Give the location of every parasitized red blood cell.
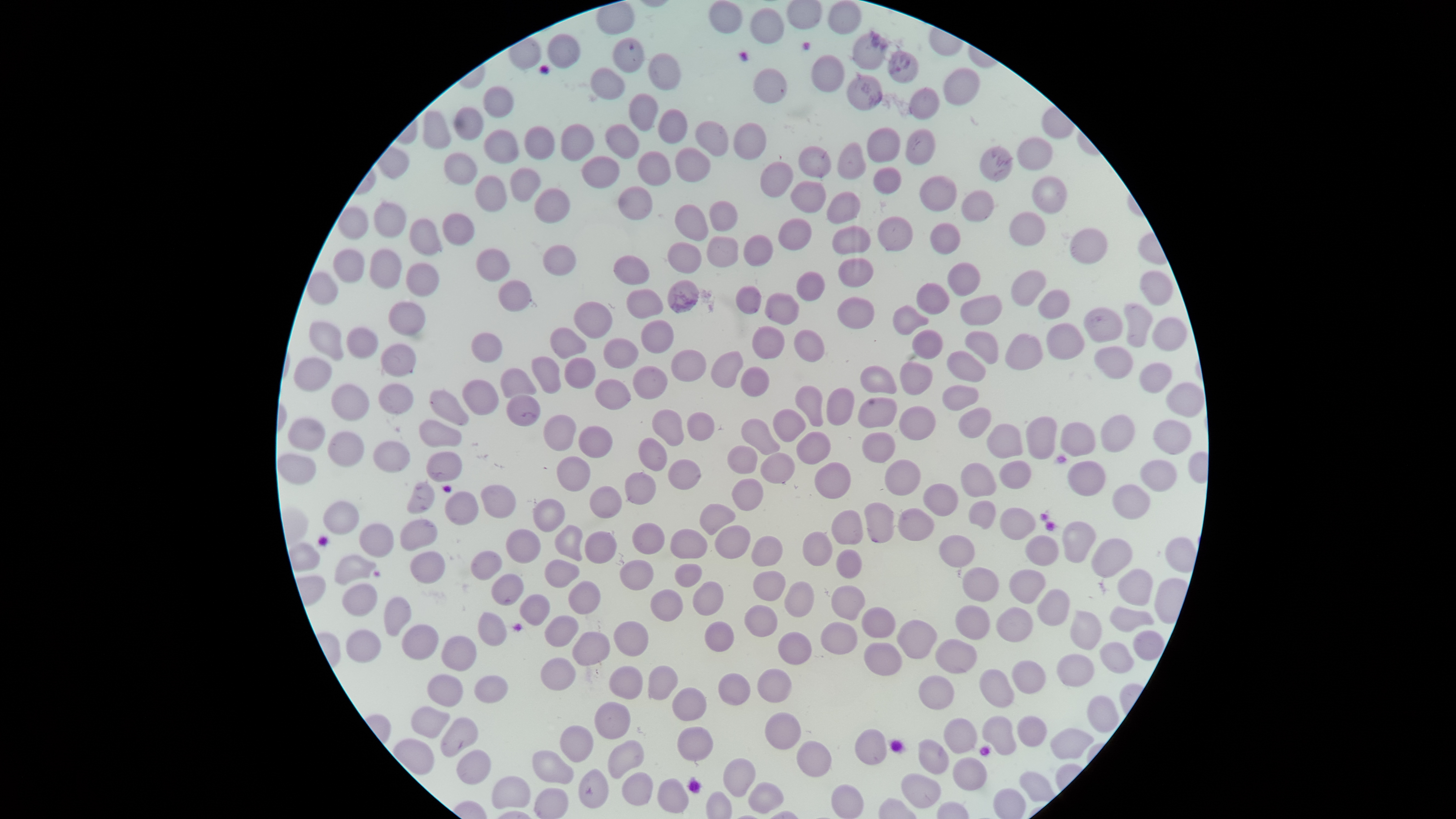
No parasitized red blood cells identified.

Approximate bounding boxes as {left, top, right, bottom} in pixels. Uninfected red blood cells: {828, 0, 863, 35}, {709, 1, 743, 34}, {750, 8, 785, 45}, {852, 32, 888, 71}, {547, 33, 580, 69}, {887, 51, 918, 84}, {648, 53, 681, 90}, {811, 55, 845, 92}, {589, 68, 625, 100}, {753, 68, 787, 104}, {943, 68, 981, 106}, {846, 75, 883, 111}, {482, 87, 515, 118}, {908, 88, 940, 121}, {628, 94, 658, 132}, {454, 107, 484, 142}, {657, 108, 687, 145}, {422, 111, 451, 150}, {694, 120, 729, 157}, {732, 122, 767, 160}, {561, 124, 594, 162}, {604, 124, 640, 158}, {523, 126, 554, 161}, {866, 128, 900, 163}, {905, 128, 935, 166}, {484, 129, 518, 165}, {1016, 137, 1053, 170}, {836, 141, 866, 180}, {798, 145, 831, 178}, {978, 146, 1013, 181}, {674, 147, 710, 182}, {637, 151, 671, 186}, {443, 152, 476, 186}, {580, 156, 620, 189}, {760, 160, 793, 198}, {509, 167, 540, 203}, {872, 167, 901, 195}, {475, 175, 506, 212}, {919, 175, 956, 212}, {1031, 175, 1067, 214}, {790, 180, 826, 213}, {618, 186, 652, 220}, {534, 188, 571, 225}, {961, 190, 994, 223}, {826, 192, 861, 224}, {709, 200, 737, 230}, {373, 201, 405, 239}, {673, 204, 709, 241}, {337, 206, 369, 240}, {1008, 211, 1044, 245}, {442, 213, 475, 246}, {876, 216, 913, 252}, {409, 218, 442, 256}, {778, 218, 811, 251}, {929, 223, 962, 255}, {832, 225, 871, 254}, {1069, 228, 1107, 264}, {742, 234, 773, 267}, {706, 236, 738, 267}, {667, 242, 703, 273}, {543, 244, 576, 276}, {476, 248, 509, 283}, {333, 249, 364, 284}, {369, 250, 401, 290}, {612, 255, 649, 284}, {837, 258, 873, 287}, {406, 262, 439, 298}, {947, 262, 981, 297}, {1140, 269, 1173, 306}, {307, 270, 338, 306}, {1010, 270, 1047, 306}, {796, 271, 825, 302}, {498, 279, 530, 312}, {667, 279, 698, 313}, {917, 283, 949, 315}, {735, 285, 762, 315}, {627, 288, 663, 319}, {1038, 289, 1070, 320}, {764, 293, 800, 326}, {960, 295, 1003, 325}, {837, 296, 874, 330}, {573, 301, 612, 339}, {388, 302, 426, 336}, {1123, 303, 1151, 348}, {893, 304, 929, 335}, {1083, 307, 1122, 343}, {1152, 317, 1187, 352}, {640, 319, 675, 354}, {309, 321, 344, 362}, {1046, 323, 1085, 359}, {751, 325, 785, 359}, {550, 327, 587, 359}, {346, 328, 379, 359}, {793, 329, 826, 362}, {911, 330, 943, 359}, {964, 330, 998, 365}, {470, 332, 502, 363}, {1004, 333, 1043, 371}, {603, 338, 638, 369}, {380, 343, 417, 378}, {1093, 346, 1133, 379}, {670, 348, 706, 382}, {711, 351, 743, 388}, {946, 351, 986, 381}, {531, 356, 561, 393}, {293, 357, 333, 392}, {564, 357, 595, 388}, {899, 361, 932, 395}, {1139, 362, 1172, 394}, {632, 365, 668, 400}, {859, 365, 897, 394}, {739, 366, 769, 397}, {500, 368, 535, 398}, {593, 378, 632, 410}, {463, 379, 498, 415}, {378, 383, 414, 415}, {1165, 383, 1204, 418}, {331, 384, 369, 421}, {794, 385, 823, 427}, {941, 385, 979, 411}, {826, 387, 854, 426}, {429, 389, 469, 427}, {506, 394, 541, 426}, {858, 397, 898, 428}, {899, 406, 936, 442}, {958, 407, 991, 439}, {651, 408, 684, 446}, {773, 408, 805, 442}, {686, 412, 715, 442}, {543, 414, 577, 451}, {1100, 414, 1136, 453}, {1025, 416, 1056, 459}, {287, 417, 325, 451}, {741, 418, 780, 456}, {419, 420, 462, 448}, {1152, 420, 1193, 456}, {1060, 422, 1095, 457}, {987, 423, 1023, 459}, {578, 425, 612, 459}, {796, 431, 831, 464}, {327, 432, 364, 467}, {861, 432, 896, 463}, {637, 437, 668, 471}, {373, 441, 410, 473}, {426, 451, 462, 483}, {277, 453, 317, 485}, {760, 453, 795, 484}, {556, 456, 590, 493}, {668, 459, 701, 490}, {1139, 459, 1177, 493}, {884, 460, 921, 495}, {999, 460, 1032, 490}, {1067, 461, 1105, 496}, {815, 462, 852, 499}, {960, 463, 996, 498}, {624, 472, 656, 505}, {730, 478, 763, 510}, {406, 482, 436, 515}, {480, 484, 516, 519}, {923, 484, 958, 516}, {1113, 484, 1151, 520}, {588, 486, 622, 518}, {445, 491, 479, 526}, {532, 499, 566, 532}, {968, 500, 996, 530}, {322, 501, 359, 535}, {864, 502, 894, 543}, {699, 504, 736, 535}, {999, 507, 1036, 541}, {897, 508, 935, 541}, {831, 509, 863, 545}, {399, 520, 439, 551}, {1063, 521, 1097, 563}, {631, 522, 665, 555}, {358, 524, 395, 558}, {553, 524, 583, 561}, {714, 525, 751, 559}, {505, 529, 540, 564}, {669, 529, 708, 560}, {584, 531, 618, 563}, {802, 531, 833, 566}, {750, 535, 783, 567}, {938, 535, 975, 567}, {1024, 536, 1060, 566}, {1091, 538, 1132, 579}, {835, 549, 862, 578}, {470, 550, 503, 581}, {410, 551, 446, 584}, {334, 554, 376, 585}, {544, 559, 580, 589}, {618, 559, 654, 591}, {674, 563, 703, 588}, {962, 567, 999, 601}, {1117, 569, 1153, 606}, {753, 570, 785, 601}, {1009, 570, 1045, 604}, {491, 573, 524, 606}, {692, 580, 724, 616}, {568, 581, 600, 615}, {783, 581, 815, 618}, {342, 583, 378, 618}, {830, 585, 866, 621}, {650, 588, 683, 622}, {1035, 589, 1070, 627}, {519, 594, 550, 626}, {383, 596, 412, 639}, {744, 604, 778, 637}, {954, 605, 991, 640}, {1109, 606, 1153, 633}, {860, 607, 895, 639}, {995, 607, 1033, 642}, {1070, 611, 1102, 650}, {477, 612, 507, 647}, {544, 615, 579, 647}, {896, 620, 937, 660}, {612, 621, 649, 657}, {703, 621, 734, 653}, {820, 621, 858, 654}, {402, 625, 439, 661}, {345, 629, 381, 664}, {1132, 630, 1164, 660}, {572, 631, 611, 666}, {778, 631, 812, 665}, {440, 636, 477, 671}, {934, 639, 977, 674}, {1099, 641, 1134, 673}, {863, 642, 903, 676}, {1057, 654, 1094, 688}, {540, 657, 575, 692}, {1011, 660, 1047, 695}, {608, 666, 643, 700}, {647, 666, 677, 701}, {757, 668, 791, 704}, {979, 670, 1014, 708}, {717, 673, 750, 706}, {426, 674, 464, 708}, {473, 675, 509, 704}, {918, 675, 955, 710}, {671, 687, 706, 721}, {1087, 696, 1120, 733}, {593, 702, 631, 739}, {410, 706, 450, 739}, {764, 712, 802, 749}, {1017, 715, 1047, 747}, {983, 716, 1017, 756}, {440, 717, 479, 756}, {943, 718, 977, 754}, {559, 725, 593, 763}, {677, 726, 713, 762}, {855, 728, 888, 765}, {1050, 728, 1093, 759}, {918, 739, 949, 775}, {607, 740, 645, 779}, {796, 740, 832, 777}, {456, 749, 491, 785}, {531, 750, 573, 785}, {952, 757, 987, 791}, {723, 758, 756, 798}, {578, 769, 609, 809}, {1019, 771, 1055, 802}, {622, 772, 653, 807}, {900, 773, 940, 809}, {491, 777, 531, 809}, {657, 778, 689, 814}, {748, 782, 784, 814}, {831, 784, 864, 818}, {534, 788, 568, 819}. Photographed with a smartphone camera through the microscope eyepiece. Image is 1456×819 pixels. Circular visible region. Thin blood smear. Giemsa stain. One field of view of the specimen.